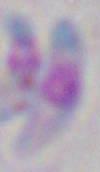

identification = Toxoplasma gondii
modality = photomicrograph
magnification = 1000x